Outline each Plasmodium ovale-infected red blood cell.
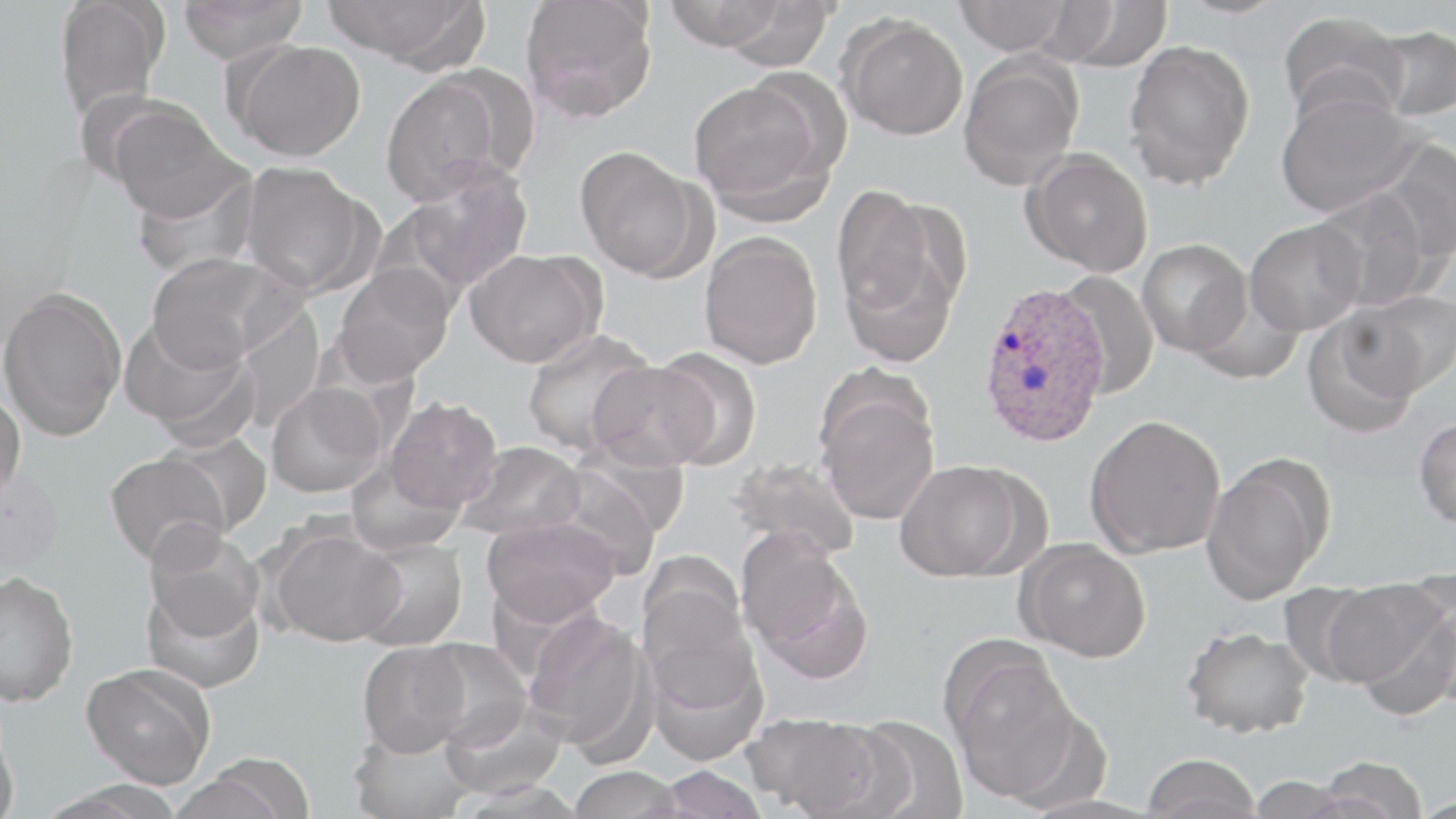

Approximate bounding boxes as (x1,y1)-(x2,y2) corner pairs in pixels.
Plasmodium ovale-infected red blood cells: (977,280)-(1111,448).

Uninfected red blood cell locations: (52,0)-(170,121), (176,0)-(310,61), (322,0)-(485,66), (519,0)-(658,123), (954,0)-(1072,54), (1172,0)-(1294,19), (663,1)-(788,51), (717,1)-(838,72), (1049,1)-(1173,72), (1278,10)-(1409,125), (838,14)-(968,140), (1370,24)-(1455,121), (229,40)-(366,161), (1123,40)-(1256,188), (958,55)-(1083,190), (379,72)-(509,205), (687,76)-(836,219), (1275,89)-(1423,217), (105,99)-(245,223), (1375,139)-(1456,262), (574,146)-(707,280), (1023,148)-(1153,277), (400,158)-(534,294), (239,161)-(375,296), (129,164)-(261,279), (832,185)-(950,323), (1311,188)-(1433,311), (1245,219)-(1367,335), (699,231)-(823,370), (1137,238)-(1251,357), (838,244)-(961,370), (465,248)-(604,367), (146,251)-(294,368), (332,264)-(455,385), (1054,270)-(1159,398), (0,286)-(127,440), (1187,286)-(1305,384), (1341,290)-(1455,398), (230,300)-(327,433), (119,312)-(256,446), (1302,313)-(1422,438), (521,327)-(657,457), (650,347)-(762,470), (588,359)-(718,471), (266,383)-(386,498), (815,383)-(940,525), (0,385)-(26,503), (384,397)-(502,514), (1085,414)-(1226,557), (1413,417)-(1456,528), (154,431)-(273,539), (568,439)-(689,541), (458,440)-(586,541), (105,451)-(233,566), (728,456)-(861,561), (345,457)-(464,557), (1201,458)-(1330,604), (895,460)-(1031,581), (544,464)-(665,579), (0,468)-(63,587), (481,516)-(619,626), (267,524)-(404,647), (142,525)-(264,645), (738,532)-(871,680), (351,537)-(468,651), (1016,538)-(1151,662), (0,571)-(79,707), (142,572)-(265,693), (637,574)-(756,707), (1322,577)-(1450,698), (1277,580)-(1383,687), (522,611)-(651,754), (1181,625)-(1314,738), (416,638)-(534,750), (358,641)-(471,756), (645,641)-(769,765), (946,650)-(1084,802), (79,664)-(215,789), (439,699)-(568,801), (746,712)-(890,817), (0,715)-(20,819), (849,715)-(970,819), (349,724)-(476,819), (1141,753)-(1263,819), (182,754)-(318,819), (1315,755)-(1429,818), (654,765)-(769,819), (567,766)-(686,819), (1246,775)-(1358,819), (453,779)-(589,817), (35,780)-(188,818). Slide-level diagnosis: Plasmodium ovale. Image is 1456×819 pixels. One field of a larger specimen. May-Grünwald-Giemsa stain. Thin blood film. Captured at 1000x magnification. Light microscopy.